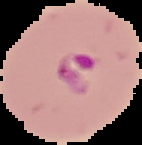
Summary:
  - Image size: 142×145 pixels
  - Image type: segmented cell region with the area outside set to black
  - Preparation: thin blood film
  - Result: malaria parasites identified